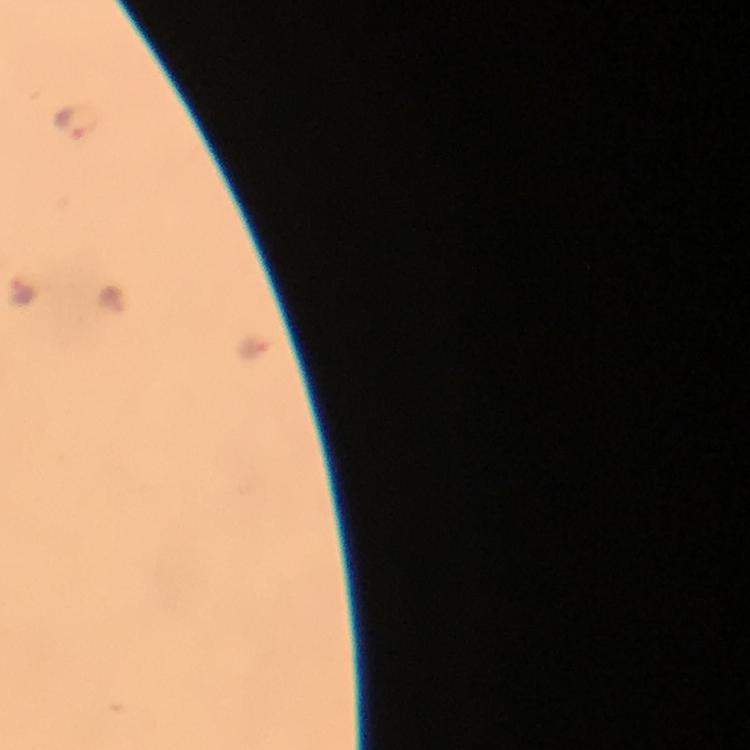 Approximate centers as (x, y) in pixels. Malaria parasite locations: (75, 121), (23, 292), (112, 299), (257, 347). Giemsa-stained preparation. Smartphone photograph taken through a microscope. From a malaria diagnostic workup. Thick blood smear. A crop from one field of view. At 100x magnification. Image is 750×750 pixels. Immersion oil applied.